State which parasite is depicted.
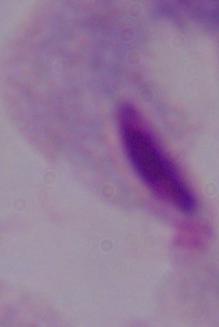
This is a trichomonad.

Summary:
  - Modality: photomicrograph
  - Magnification: 1000x